Classify this cell by malaria status.
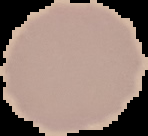
Uninfected.

preparation: thin blood film
image_type: cell region segmented out of the field of view; surrounding area masked to black
image_size: 148×136 pixels